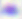

Toxoplasma gondii is seen. Captured at 400x magnification. Photomicrograph.